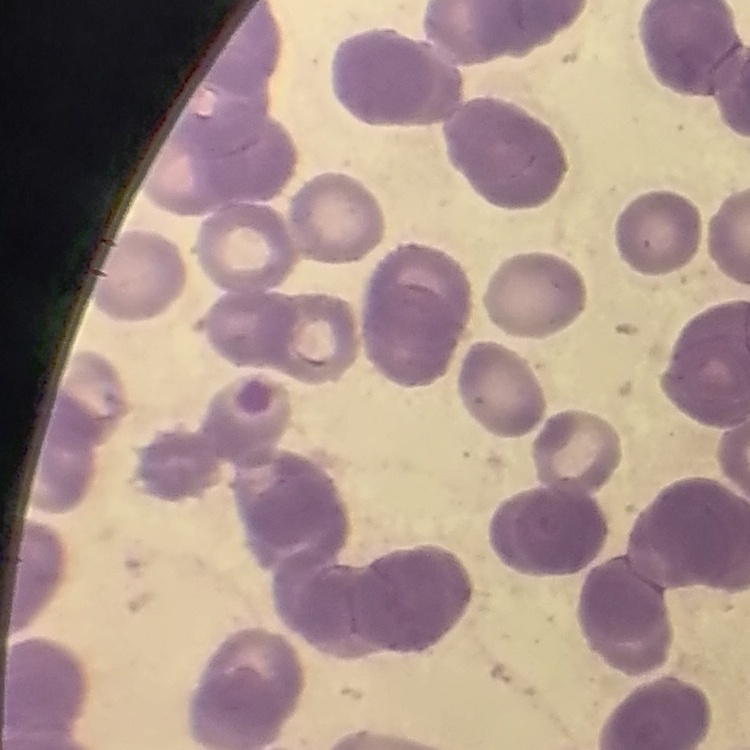

red_blood_cell_morphology: rouleaux formation
preparation: thin blood smear
stain: Field's or Giemsa
image_type: one tile cut from a larger photomicrograph